Mark where leukocytes are.
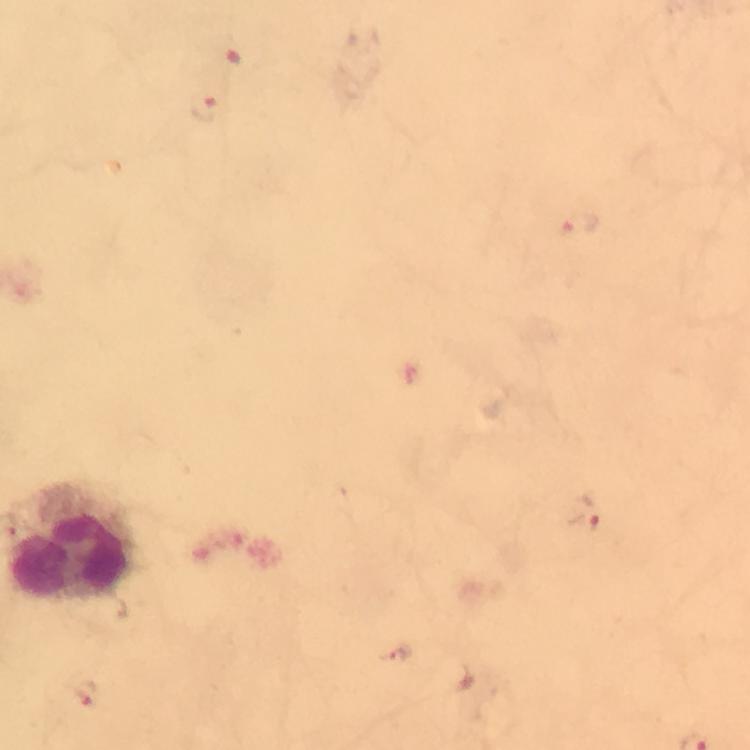

Approximate centers as {x, y} in pixels.
Leukocytes: {68, 544}.

Malaria parasite locations: {204, 108}, {582, 226}, {585, 514}, {84, 694}. Thick smear. From a malaria diagnostic workup. At 100x magnification. Giemsa-stained preparation. Smartphone photograph taken through a microscope. Image is 750×750 pixels. Cropped region of a single field of view. Immersion oil was used.